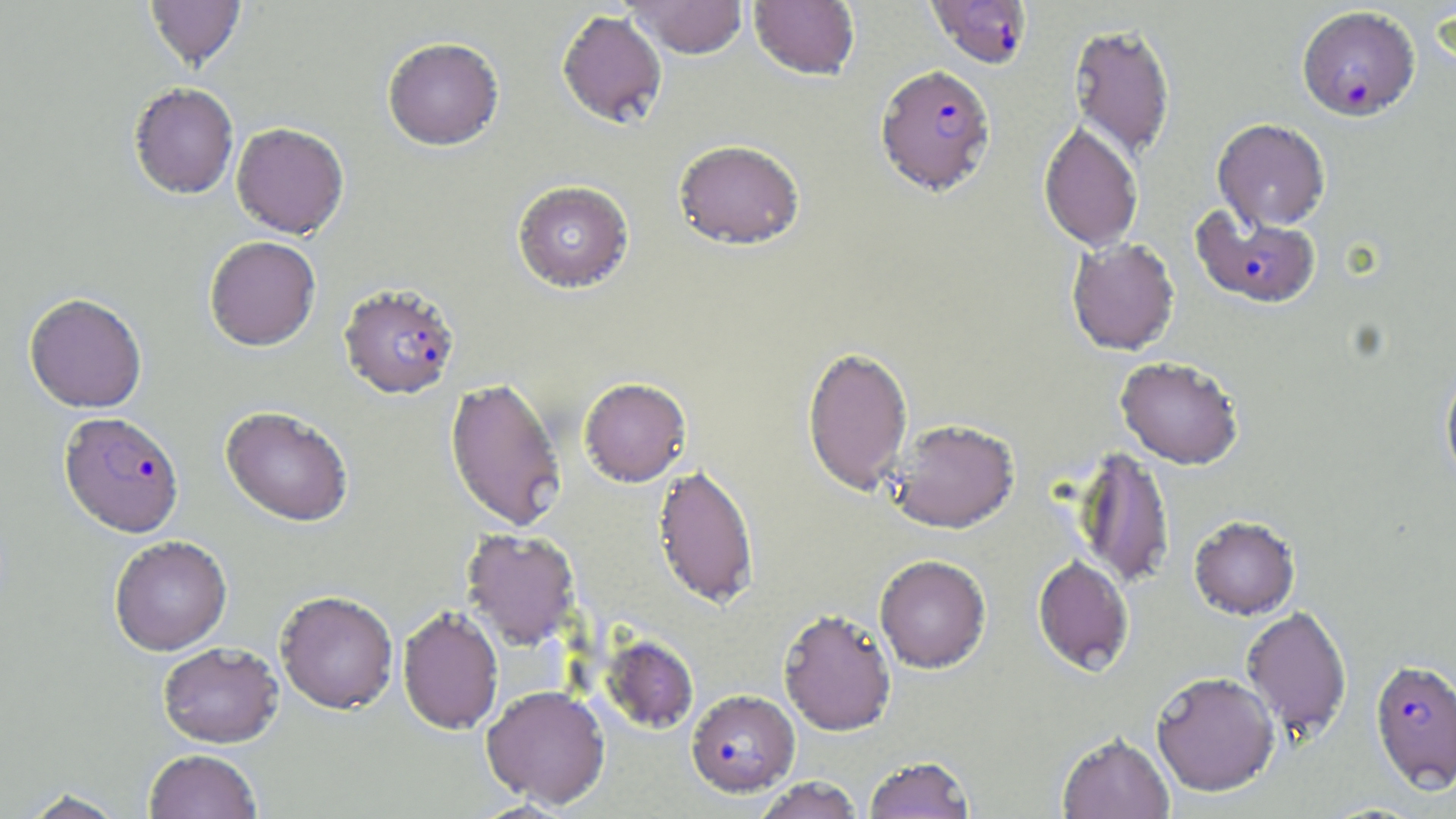
Plasmodium falciparum-infected red blood cell locations = approximate bounding boxes as (x1, y1, x2, y2) in pixels: (926, 0, 1033, 69), (1297, 5, 1420, 121), (875, 64, 996, 196), (1190, 204, 1322, 309), (339, 283, 460, 399), (59, 411, 184, 537), (1369, 659, 1456, 791), (686, 689, 800, 796)
slide-level diagnosis = Plasmodium falciparum
modality = optical microscopy
image size = 1456×819 pixels
field of view = single
magnification = 1000x
stain = May-Grünwald-Giemsa
preparation = thin blood smear
uninfected red blood cell locations = approximate bounding boxes as (x1, y1, x2, y2) in pixels: (145, 0, 246, 70), (625, 0, 748, 60), (748, 0, 860, 81), (557, 10, 667, 129), (1068, 22, 1177, 161), (382, 36, 505, 152), (128, 82, 239, 199), (1213, 118, 1330, 231), (1038, 121, 1143, 251), (231, 122, 349, 238), (673, 139, 806, 251), (512, 180, 634, 293), (204, 236, 321, 351), (1065, 237, 1180, 356), (24, 292, 147, 413), (802, 345, 913, 497), (1115, 356, 1244, 469), (1439, 363, 1456, 491), (444, 376, 567, 533), (578, 377, 691, 487), (220, 406, 354, 527), (888, 419, 1019, 533), (1073, 446, 1175, 590), (651, 464, 760, 609), (1188, 514, 1301, 620), (461, 529, 581, 649), (109, 535, 233, 656), (874, 555, 992, 673), (1032, 555, 1134, 676), (275, 590, 399, 714), (1241, 605, 1353, 741), (397, 606, 504, 735), (778, 608, 897, 736), (600, 635, 699, 734), (157, 641, 284, 748), (1151, 672, 1280, 797), (481, 684, 610, 809), (1056, 732, 1175, 819), (144, 749, 263, 819), (863, 756, 975, 819), (752, 776, 865, 819), (18, 787, 129, 818)